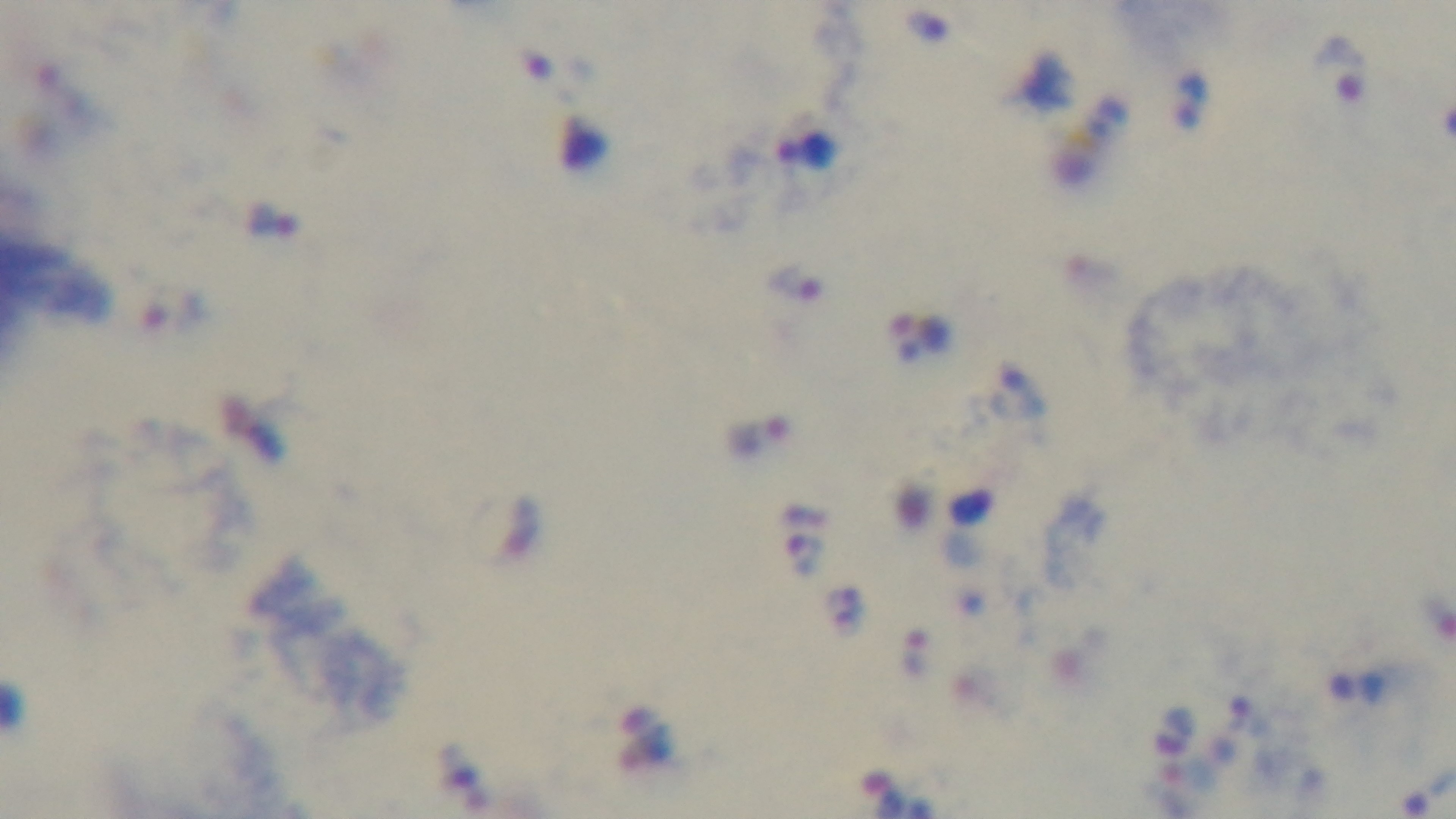
{
  "objective": "100x oil immersion",
  "capture": "mounted 4K digital camera",
  "preparation": "thick smear",
  "stain": "Giemsa",
  "field_of_view": "single",
  "modality": "light microscopy",
  "malaria_status": "positive"
}